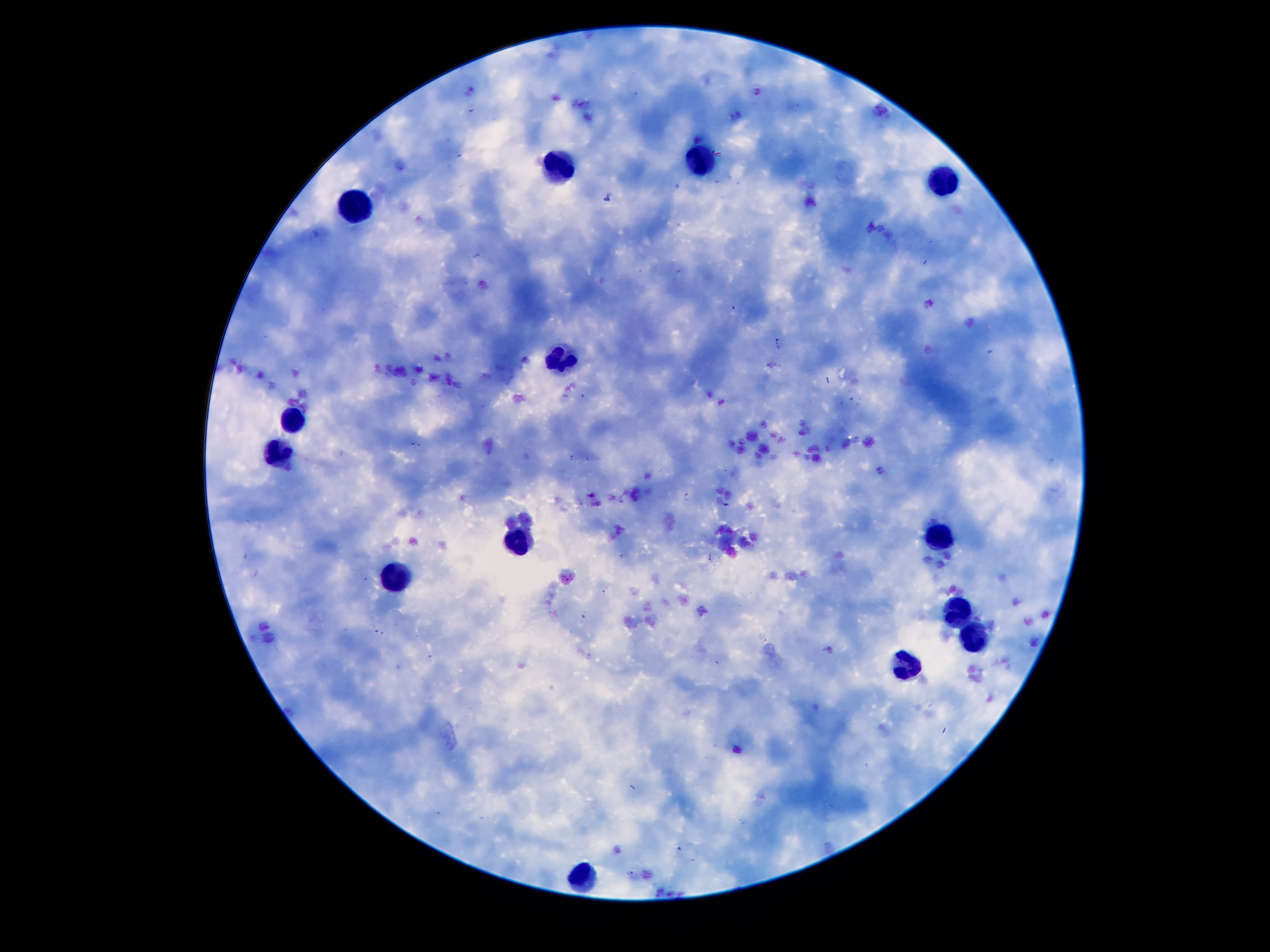
Approximate centers as [x, y] in pixels.
Summary:
  - Leukocyte locations: [703, 160], [552, 168], [943, 181], [355, 207], [559, 361], [293, 421], [279, 455], [944, 539], [516, 542], [398, 577], [956, 612], [975, 634], [909, 665], [581, 873]
  - Malaria parasite locations: [608, 195], [779, 343], [416, 443], [687, 498]
  - Preparation: thick blood film
  - Magnification: 100x
  - Capture: smartphone camera through the microscope eyepiece
  - Image size: 1270×952 pixels
  - Stain: Giemsa
  - Patient malaria status: infected with Plasmodium falciparum
  - Field of view: single